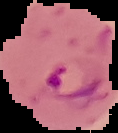

image type = segmented cell region with the area outside set to black
result = malaria parasites identified
image size = 118×133 pixels
preparation = thin blood film